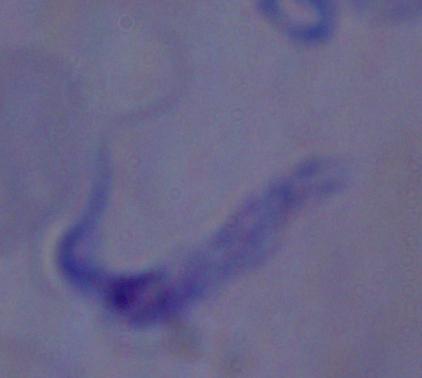 Captured at 1000x magnification. A trypanosome is shown. Micrograph.